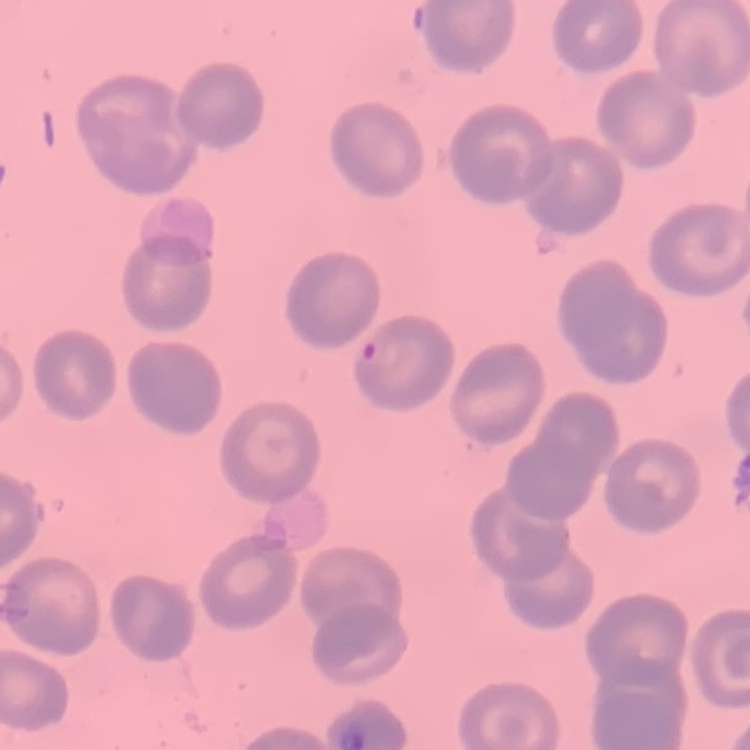

Summary:
  - Red blood cell morphology: no rouleaux formation
  - Image type: square crop of a larger photomicrograph
  - Preparation: thin blood smear
  - Stain: Field's or Giemsa